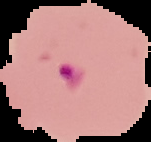
Summary:
  - Image type: segmented cell region on a black background
  - Preparation: thin blood film
  - Image size: 151×142 pixels
  - Result: malaria parasites detected